Comment on the morphology of the red blood cells.
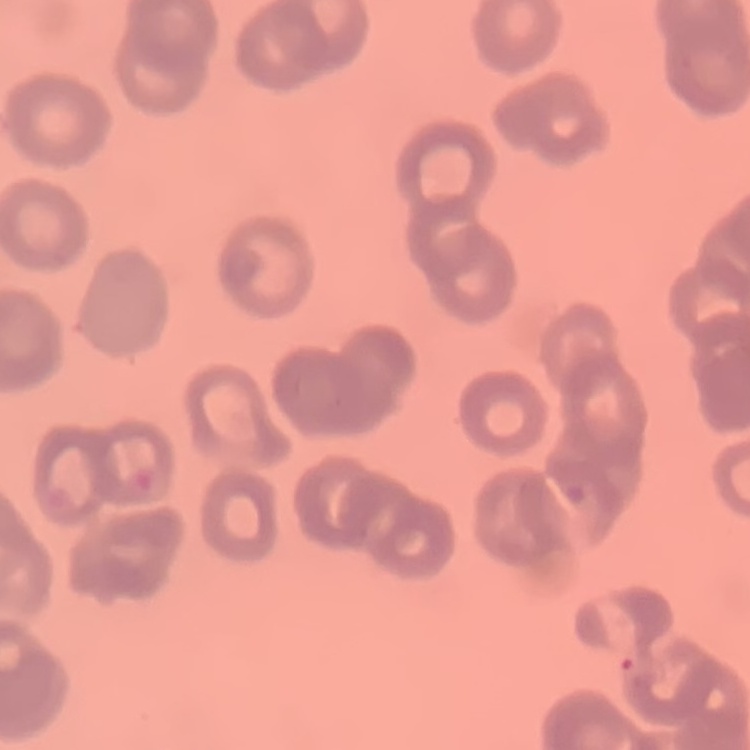

They show rouleaux formation.

image type = square crop of a larger photomicrograph
stain = Field's or Giemsa
preparation = thin blood smear